Report the malaria status.
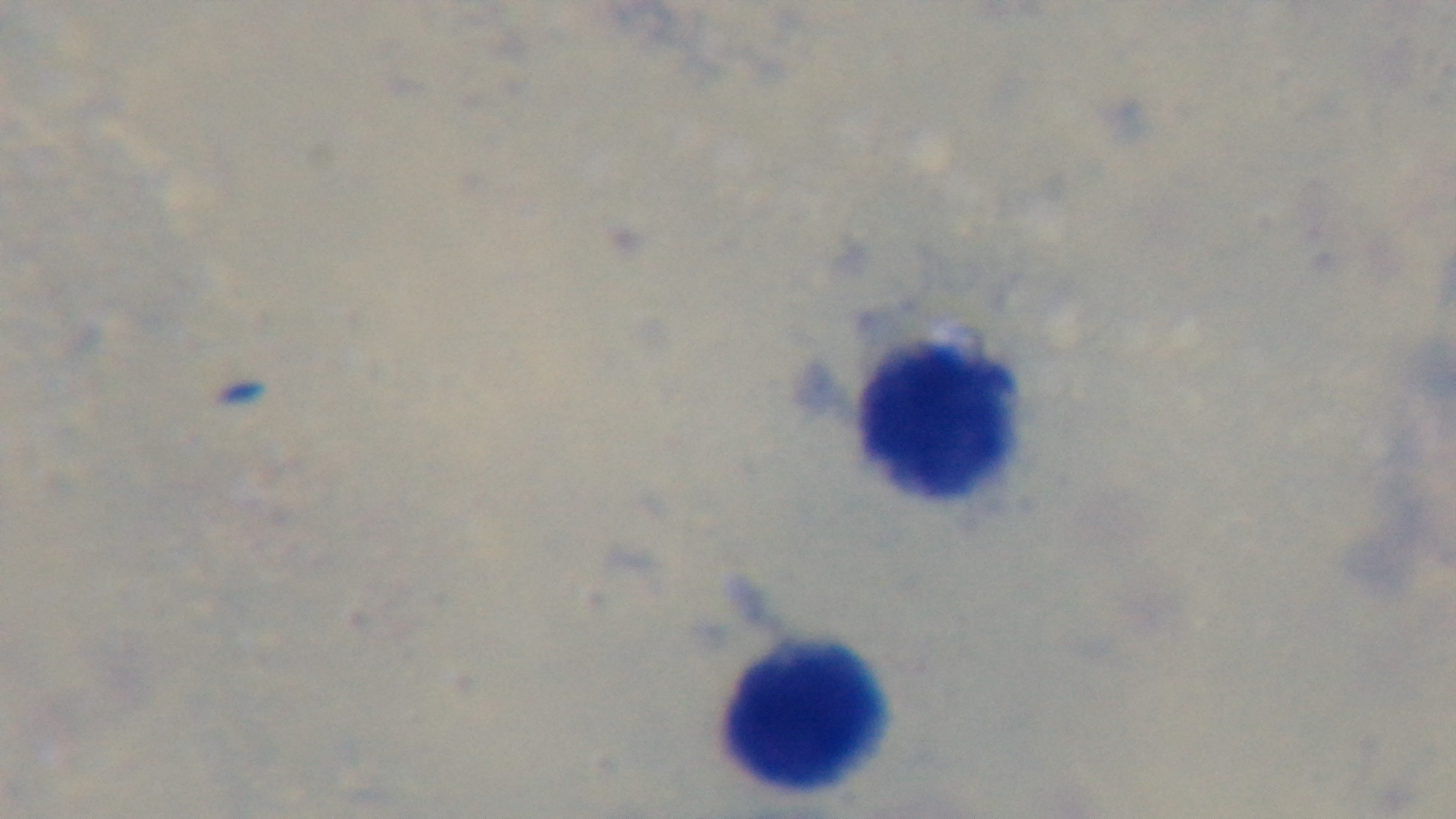

It is uninfected.

100x oil-immersion objective. Giemsa stain. Photomicrograph. Preparation: thick blood film. Captured with a mounted 4K digital camera. One field from the slide.